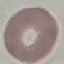
Result: no malaria parasites seen. Giemsa-stained preparation. Cell patch, automatically extracted from a larger field of view and resized to 64 × 64 pixels. Thin blood smear. Acquired by smartphone through the microscope eyepiece.